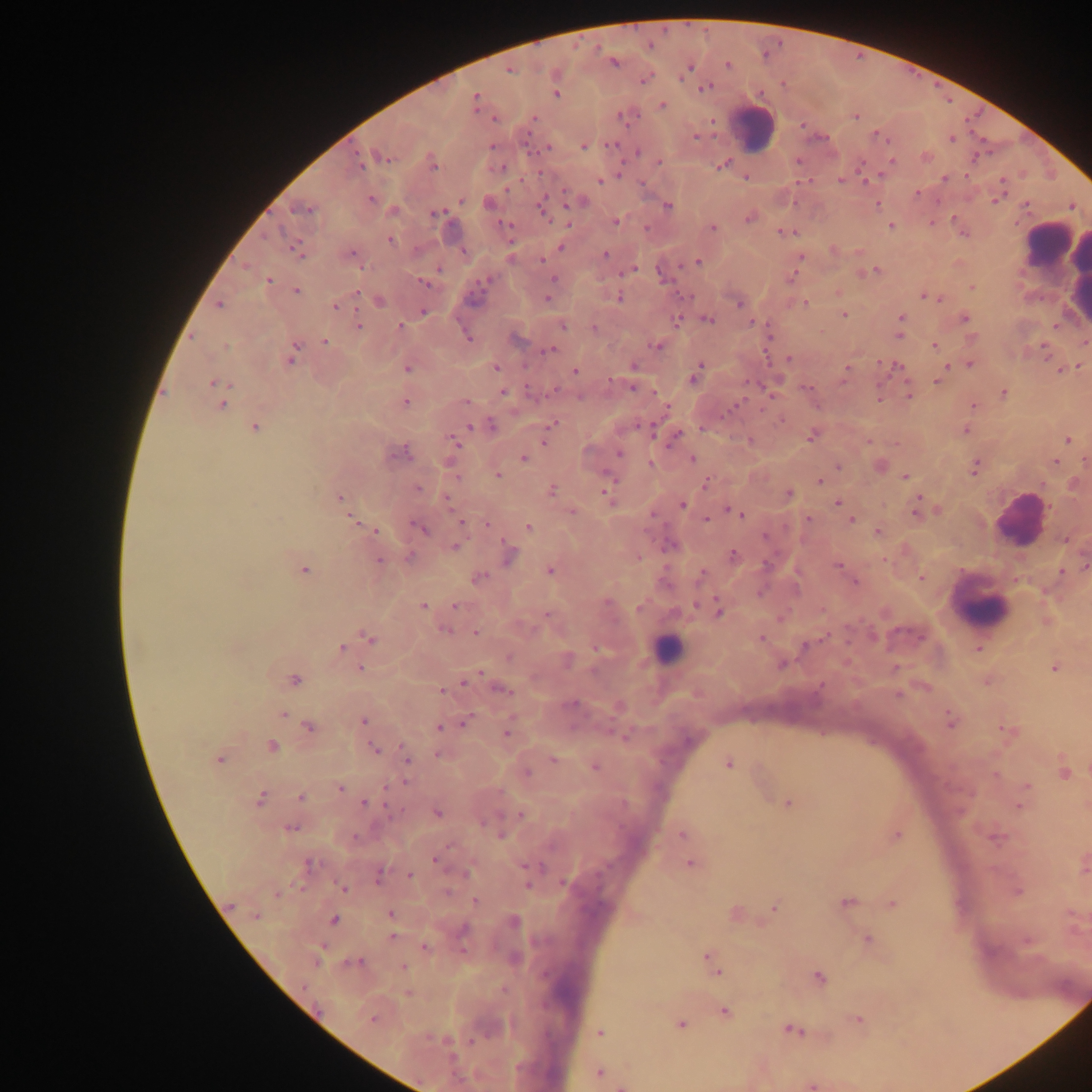

Approximate centers as [x, y] in pixels.
Summary:
  - Leukocyte locations: [754, 128], [1048, 245], [1053, 261], [1019, 520], [982, 606], [667, 649]
  - Malaria parasite locations: [614, 61], [727, 65], [689, 67], [509, 70], [644, 80], [705, 87], [556, 93], [476, 100], [661, 105], [621, 115], [855, 116], [494, 118], [533, 118], [695, 136], [952, 139], [583, 146], [547, 147], [638, 152], [381, 156], [926, 157], [358, 159], [890, 161], [431, 162], [658, 162], [723, 163], [746, 176], [944, 178], [599, 180], [841, 180], [865, 181], [1002, 182], [917, 193], [369, 199], [995, 200], [580, 201], [488, 202], [876, 204], [667, 205], [303, 208], [542, 208], [392, 210], [435, 213], [750, 217], [615, 221], [891, 225], [711, 228], [785, 232], [390, 239], [560, 247], [296, 249], [834, 250], [604, 254], [351, 256], [799, 259], [698, 261], [632, 268], [438, 269], [875, 270], [791, 277], [554, 279], [269, 280], [425, 282], [972, 287], [296, 291], [838, 292], [924, 295], [618, 297], [937, 297], [547, 298], [379, 300], [739, 302], [805, 303], [219, 304], [335, 305], [422, 312], [844, 314], [901, 317], [964, 318], [707, 319], [676, 321], [753, 322], [358, 325], [562, 325], [400, 326], [593, 328], [899, 335], [467, 337], [515, 337], [325, 342], [1083, 342], [656, 345], [934, 345], [1044, 348], [550, 349], [292, 356], [790, 359], [970, 362], [1079, 365], [634, 366], [947, 366], [495, 367], [408, 368], [896, 368], [846, 370], [1060, 370], [575, 371], [942, 373], [695, 375], [937, 381], [215, 384], [632, 386], [807, 387], [218, 389], [502, 391], [1003, 393], [909, 396], [879, 398], [405, 401], [465, 401], [221, 403], [972, 405], [780, 420], [553, 423], [490, 425], [254, 426], [965, 430], [675, 436], [811, 436], [546, 439], [750, 440], [1068, 440], [455, 442], [399, 452], [619, 454], [524, 458], [691, 460], [1054, 462], [650, 463], [838, 466], [879, 466], [974, 467], [498, 475], [904, 476], [819, 481], [705, 482], [1074, 483], [417, 488], [551, 490], [608, 494], [788, 494], [339, 498], [447, 501], [838, 502], [682, 504], [917, 509], [571, 511], [733, 511], [740, 514], [706, 519], [808, 519], [851, 520], [460, 522], [487, 523], [419, 527], [528, 527], [374, 531], [878, 531], [1065, 539], [455, 546], [509, 555], [733, 555], [409, 557], [883, 559], [379, 561], [839, 565], [1085, 565], [303, 569], [550, 570], [1061, 571], [702, 573], [477, 577], [921, 577], [855, 582], [423, 606], [456, 606], [718, 610], [547, 616], [445, 630], [476, 633], [367, 637], [760, 638], [805, 645], [341, 648], [978, 648], [567, 659], [782, 663], [1054, 667], [360, 668], [471, 676], [294, 679], [987, 681], [501, 688], [441, 690], [618, 706], [283, 715], [951, 720], [362, 721], [466, 721], [309, 726], [439, 726], [507, 731], [1008, 731], [271, 746], [374, 749], [440, 754], [406, 758], [218, 759], [553, 760], [728, 764], [595, 765], [1064, 771], [525, 773], [1026, 786], [340, 787], [301, 797], [259, 799], [365, 803], [788, 803], [1020, 805], [436, 812], [521, 814], [290, 827], [683, 834], [896, 834], [994, 837], [436, 859], [689, 862], [1083, 863], [309, 864], [379, 875], [410, 876], [343, 889], [1016, 890], [476, 901], [847, 901], [892, 903], [776, 905], [734, 912], [389, 915], [333, 919], [513, 922], [392, 936], [867, 940], [1026, 940], [423, 948], [711, 960], [358, 962], [403, 967], [714, 968], [818, 977], [723, 1011], [373, 1018], [857, 1019], [680, 1024], [792, 1029], [600, 1032], [599, 1073], [811, 1084], [623, 1086]
  - Capture: mobile-phone photograph through a microscope
  - Country: Ghana
  - Field of view: single
  - Image size: 1092×1092 pixels
  - Preparation: thick blood film